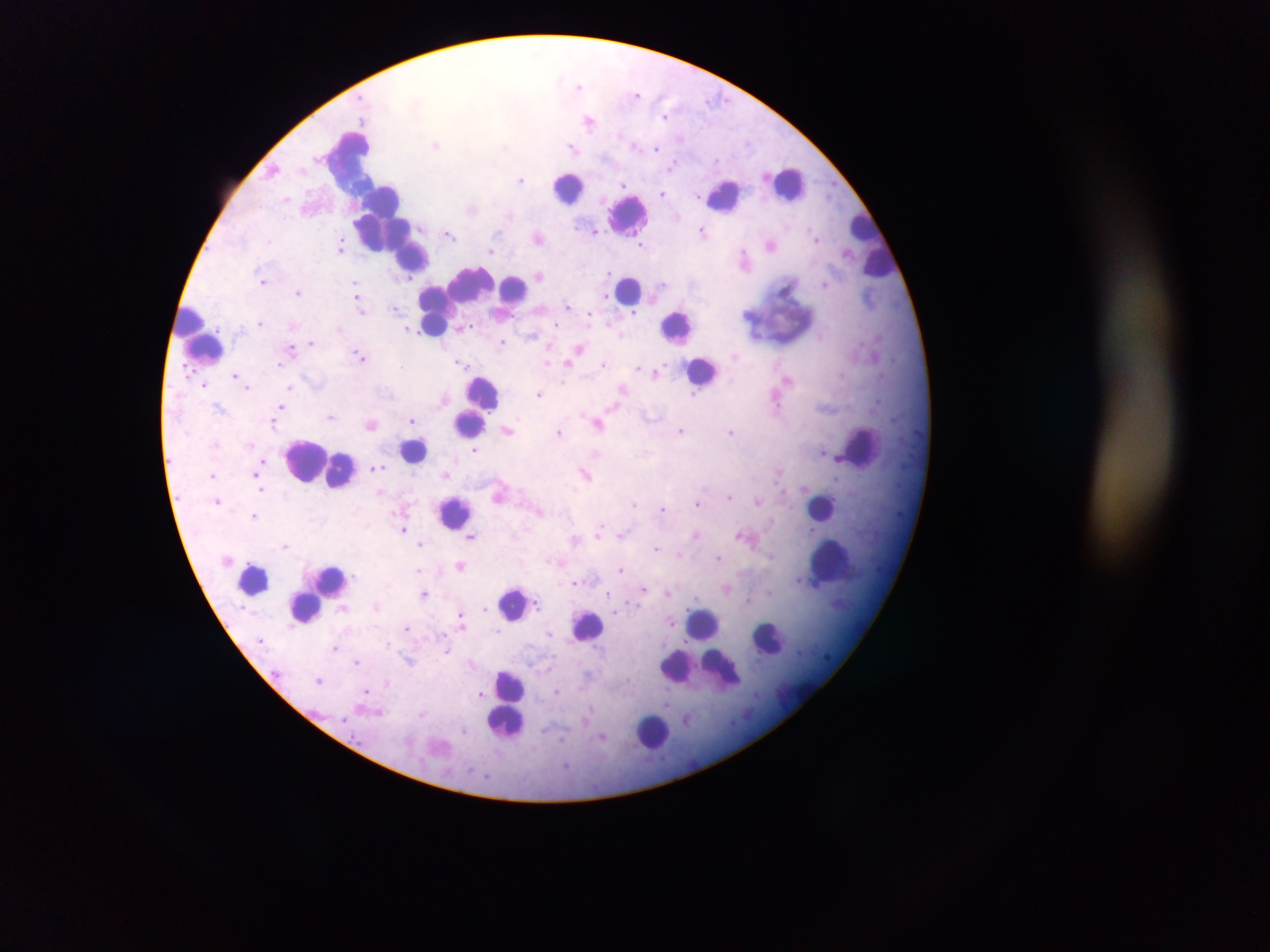

Approximate centers as {x, y} in pixels. Leukocyte locations: {347, 163}, {788, 183}, {569, 186}, {726, 195}, {628, 215}, {383, 217}, {860, 224}, {413, 258}, {879, 260}, {515, 287}, {629, 290}, {492, 291}, {460, 298}, {437, 306}, {783, 308}, {188, 323}, {433, 326}, {678, 327}, {206, 348}, {703, 370}, {484, 393}, {469, 424}, {863, 446}, {415, 450}, {313, 460}, {338, 469}, {821, 505}, {454, 513}, {828, 554}, {254, 578}, {332, 581}, {512, 603}, {306, 607}, {588, 624}, {704, 624}, {770, 638}, {721, 669}, {676, 670}, {512, 685}, {506, 722}, {653, 732}. Malaria parasite locations: {579, 85}, {636, 93}, {712, 99}, {666, 116}, {589, 121}, {634, 143}, {436, 144}, {505, 145}, {572, 146}, {657, 147}, {674, 164}, {273, 169}, {521, 179}, {625, 184}, {662, 194}, {698, 196}, {287, 199}, {472, 209}, {595, 230}, {703, 232}, {449, 234}, {538, 237}, {816, 238}, {269, 241}, {771, 244}, {341, 245}, {642, 245}, {491, 251}, {743, 258}, {609, 273}, {539, 275}, {409, 276}, {263, 281}, {356, 284}, {662, 284}, {825, 284}, {298, 292}, {606, 297}, {357, 299}, {567, 305}, {395, 309}, {360, 310}, {632, 313}, {590, 316}, {260, 323}, {339, 329}, {409, 329}, {531, 334}, {821, 336}, {502, 341}, {312, 342}, {292, 347}, {578, 349}, {360, 356}, {572, 360}, {547, 361}, {462, 363}, {567, 363}, {279, 364}, {602, 364}, {402, 367}, {638, 368}, {657, 372}, {236, 375}, {788, 379}, {246, 385}, {204, 386}, {289, 387}, {622, 388}, {539, 394}, {693, 394}, {776, 403}, {281, 407}, {219, 408}, {332, 416}, {412, 420}, {274, 423}, {370, 424}, {598, 424}, {507, 430}, {681, 431}, {559, 432}, {731, 432}, {251, 445}, {475, 451}, {377, 467}, {258, 472}, {213, 474}, {446, 474}, {586, 474}, {258, 482}, {259, 488}, {729, 496}, {217, 501}, {758, 501}, {634, 503}, {698, 503}, {663, 508}, {539, 511}, {254, 515}, {601, 528}, {403, 529}, {621, 534}, {697, 534}, {741, 535}, {472, 537}, {575, 540}, {285, 544}, {420, 544}, {657, 548}, {679, 555}, {719, 558}, {549, 561}, {461, 565}, {621, 569}, {419, 570}, {574, 582}, {644, 589}, {727, 589}, {425, 593}, {609, 593}, {668, 593}, {748, 600}, {537, 605}, {376, 606}, {485, 608}, {460, 615}, {672, 622}, {407, 629}, {497, 631}, {550, 633}, {387, 642}, {335, 647}, {447, 651}, {409, 661}, {357, 662}, {319, 679}, {387, 683}, {366, 691}, {557, 691}, {481, 694}, {379, 712}, {687, 718}, {465, 731}, {603, 737}, {562, 740}, {566, 766}. Image is 1270×952 pixels. Thick blood film. Collected in Ghana. Mobile-phone photograph taken through the microscope. Single field of view.